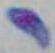

Summary:
  - Identification: Toxoplasma gondii
  - Modality: photomicrograph
  - Magnification: 1000x